State which cell type is depicted.
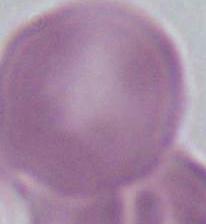
This is an erythrocyte.

magnification = 1000x
modality = photomicrograph